State the blood parasite species.
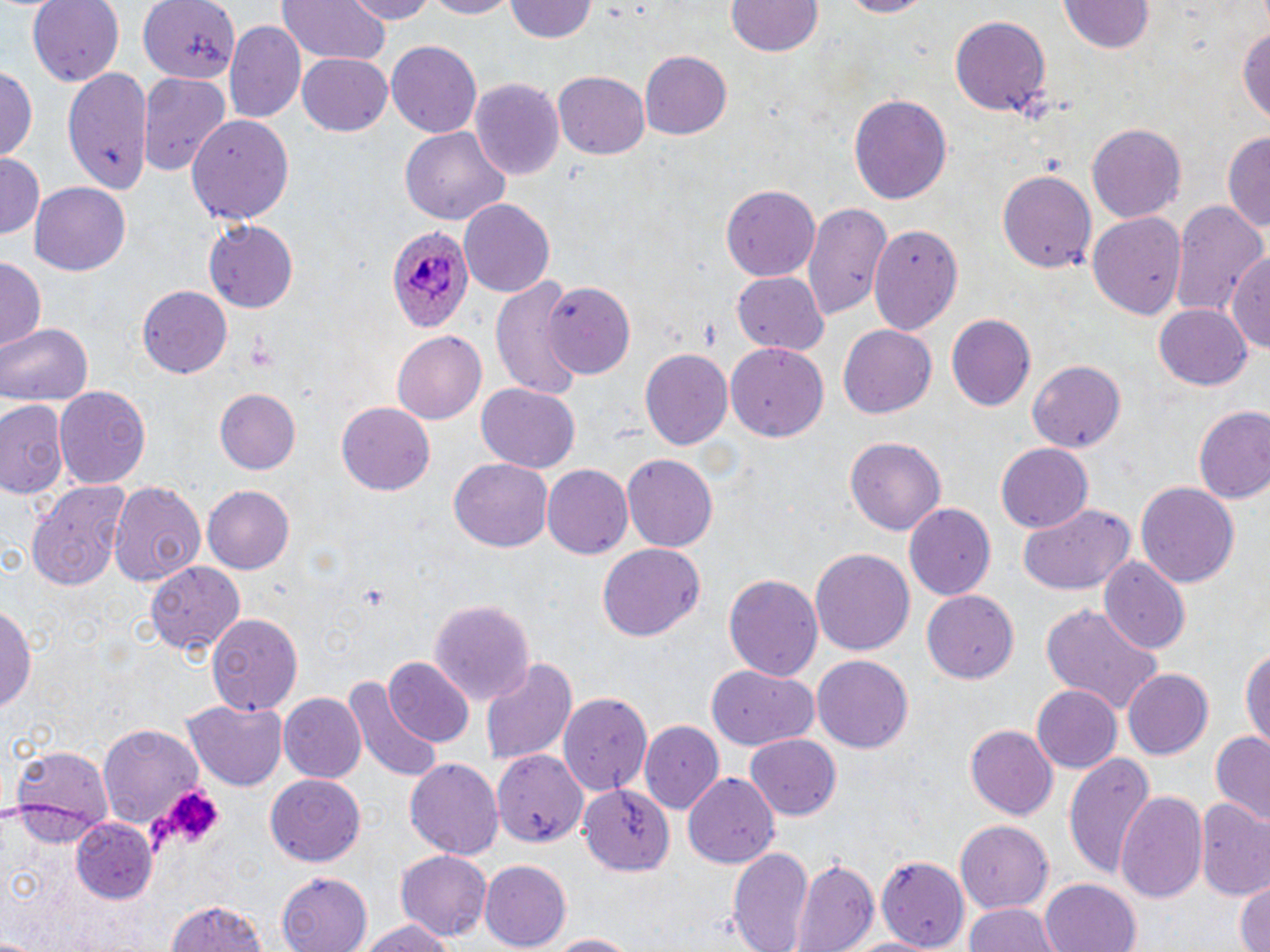
Plasmodium ovale.

Approximate bounding boxes as (x1,y1)-(x2,y2) corner pairs in pixels. Platelet locations: (153,786)-(225,852). Plasmodium ovale-infected red blood cell locations: (386,226)-(475,335). Uninfected red blood cell locations: (28,0)-(123,86), (139,0)-(243,81), (277,0)-(393,65), (340,0)-(443,23), (417,0)-(521,19), (507,0)-(597,44), (726,0)-(825,58), (830,0)-(932,18), (1058,0)-(1156,55), (948,16)-(1052,118), (1240,18)-(1270,127), (225,20)-(306,127), (386,40)-(482,136), (640,50)-(733,139), (296,52)-(391,136), (0,65)-(36,162), (65,69)-(152,194), (138,72)-(229,178), (552,72)-(651,159), (469,78)-(564,179), (848,93)-(952,207), (187,111)-(297,225), (1086,123)-(1186,224), (399,128)-(511,227), (1223,132)-(1270,240), (0,156)-(44,236), (997,169)-(1097,277), (30,182)-(131,275), (722,185)-(819,283), (458,198)-(557,298), (1171,199)-(1266,317), (803,200)-(893,321), (1088,211)-(1187,322), (203,219)-(298,312), (871,223)-(962,332), (1226,245)-(1270,351), (0,257)-(45,349), (733,271)-(830,355), (488,276)-(584,397), (546,280)-(638,377), (137,282)-(232,375), (1152,304)-(1255,391), (946,313)-(1037,413), (0,321)-(93,407), (837,324)-(936,419), (391,331)-(487,425), (727,344)-(830,439), (640,347)-(733,450), (1026,359)-(1125,453), (476,385)-(580,472), (56,387)-(150,491), (215,389)-(301,474), (0,397)-(70,502), (336,401)-(436,496), (1195,405)-(1270,508), (846,437)-(946,539), (995,443)-(1092,531), (624,454)-(718,553), (448,460)-(554,552), (543,463)-(635,559), (106,477)-(206,588), (25,478)-(137,592), (1135,481)-(1239,590), (202,485)-(294,574), (1019,503)-(1136,596), (904,504)-(996,602), (597,544)-(706,643), (811,548)-(915,658), (1101,559)-(1190,655), (146,560)-(246,657), (723,573)-(823,685), (924,589)-(1020,684), (428,598)-(535,706), (0,600)-(37,717), (1039,604)-(1168,715), (204,612)-(304,716), (1240,641)-(1269,754), (812,653)-(914,753), (479,655)-(579,768), (383,657)-(473,749), (708,665)-(820,750), (1121,668)-(1214,760), (341,674)-(444,784), (1030,685)-(1122,773), (559,691)-(654,795), (279,692)-(367,785), (184,700)-(287,791), (641,720)-(725,814), (99,724)-(205,827), (965,724)-(1058,821), (1209,730)-(1270,825), (744,735)-(843,820), (10,745)-(115,835), (491,750)-(589,853), (1062,752)-(1156,879), (405,755)-(502,856), (684,773)-(779,870), (264,774)-(367,868), (581,786)-(674,876), (1115,789)-(1208,905), (1194,799)-(1270,900), (71,818)-(157,904), (956,820)-(1055,913), (727,843)-(815,952), (396,850)-(494,941), (791,853)-(879,951), (876,855)-(969,948), (479,861)-(571,948), (277,872)-(372,952), (1234,877)-(1269,952), (1038,879)-(1142,952), (162,899)-(272,952), (961,900)-(1057,952), (355,917)-(453,952), (539,931)-(647,951), (848,934)-(941,952). Captured at 1000x magnification. Thin blood film. May-Grünwald-Giemsa-stained preparation. Optical microscopy. Single field of view. Image is 1270×952 pixels.